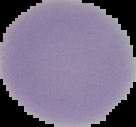
{
  "malaria_status": "uninfected",
  "image_size": "136×127 pixels",
  "image_type": "segmented cell region on a black background",
  "preparation": "thin blood smear"
}